Mark where platelets are.
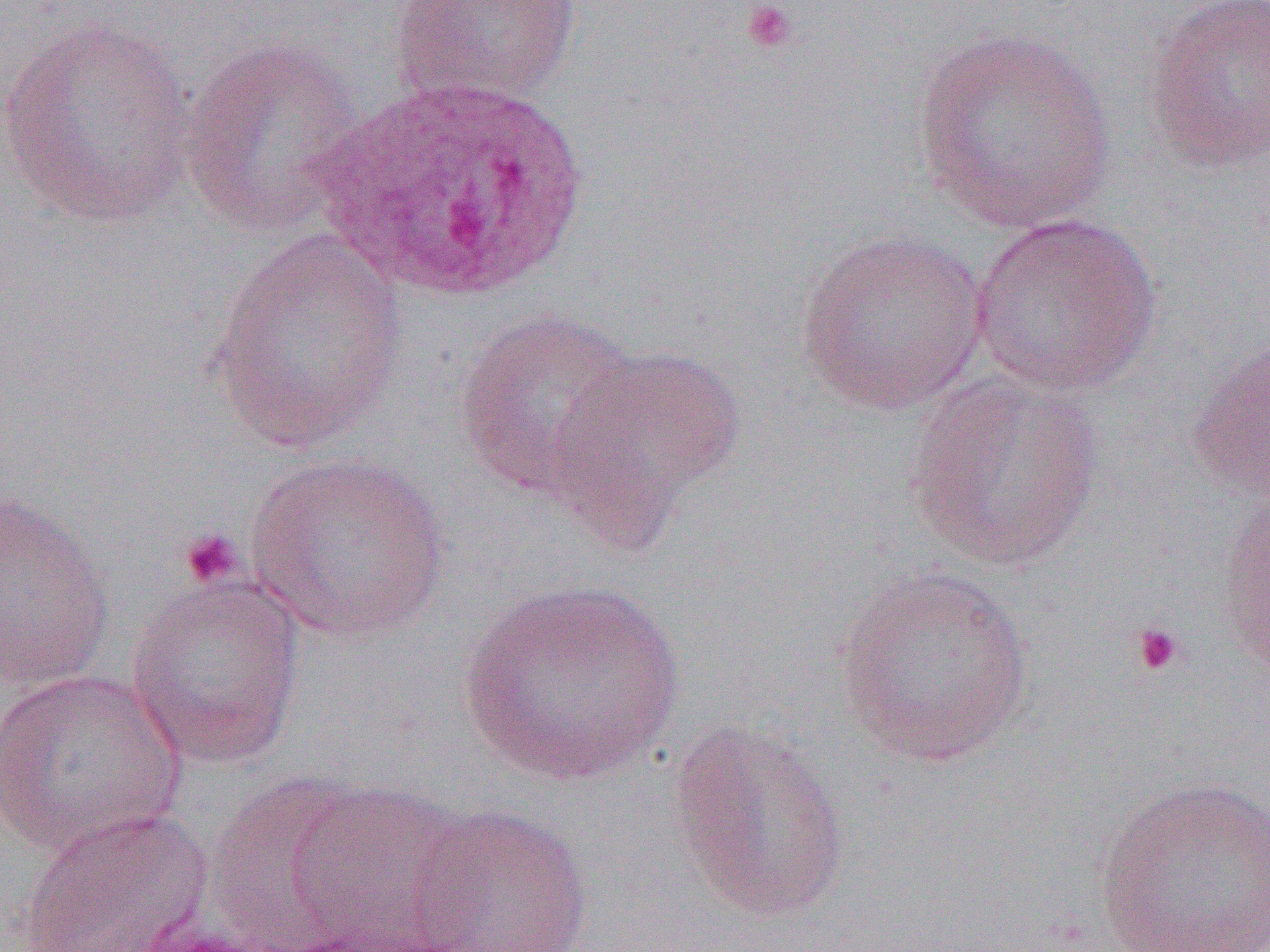

Approximate bounding boxes as [x1, y1, x2, y2] in pixels.
Platelets: [739, 0, 800, 56], [179, 526, 245, 589], [1130, 622, 1185, 677].

Uninfected red blood cell locations: [390, 1, 583, 109], [1142, 1, 1270, 173], [1, 17, 201, 228], [911, 24, 1118, 235], [178, 34, 367, 240], [968, 213, 1163, 397], [206, 229, 411, 450], [795, 229, 990, 416], [454, 309, 642, 502], [1189, 330, 1269, 502], [544, 344, 746, 546], [905, 371, 1107, 573], [246, 451, 451, 643], [1216, 477, 1270, 686], [0, 486, 116, 694], [833, 565, 1036, 767], [125, 573, 307, 770], [462, 578, 683, 788], [1, 668, 187, 858], [666, 717, 853, 926], [205, 773, 370, 948], [1094, 775, 1270, 951], [284, 780, 468, 950], [405, 803, 594, 952], [14, 807, 215, 952]. White blood cell locations: [309, 74, 597, 307]. Slide-level diagnosis: Plasmodium ovale. Image is 1270×952 pixels. Single field of view. Captured at 1000x magnification. Optical microscopy. Thin blood film.